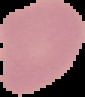 Image is 85×97 pixels. From a thin blood film. Malaria status: uninfected. Segmented cell region on a black background.